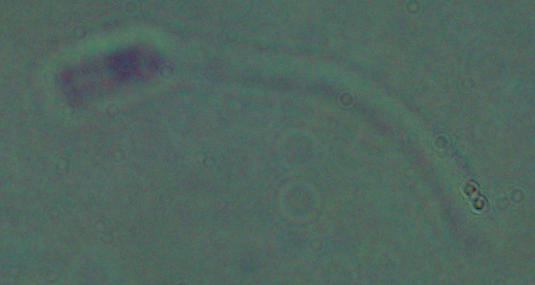
A Leishmania parasite is shown. Photomicrograph. Captured at 1000x magnification.